Outline each blood parasite and name the species.
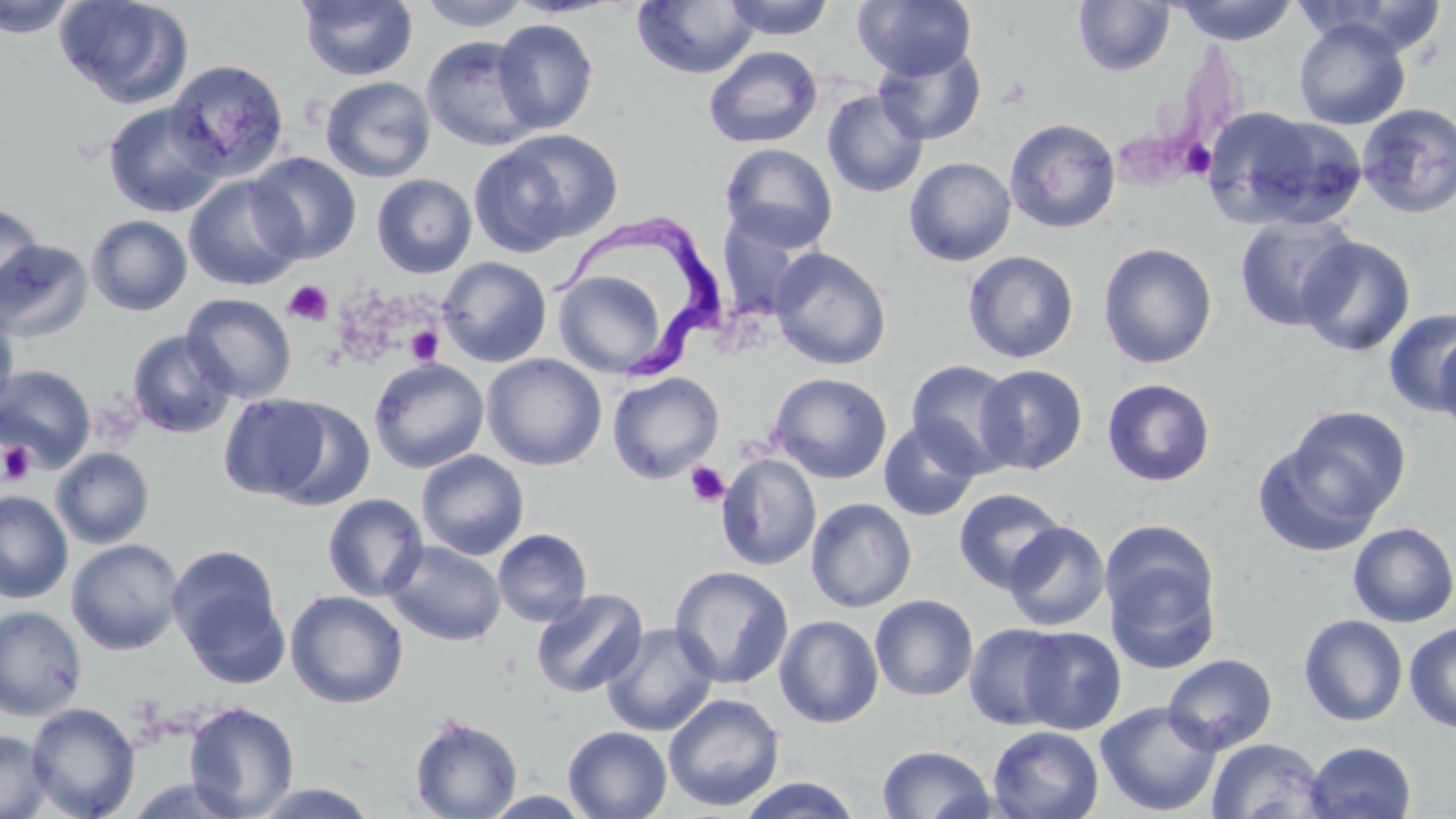
Approximate bounding boxes as [x1, y1, x2, y2] in pixels.
Trypanosoma brucei: [556, 214, 731, 383].
No Plasmodium falciparum, Plasmodium ovale, Plasmodium malariae, Plasmodium vivax, or Babesia divergens observed.

slide-level diagnosis = Trypanosoma brucei
field of view = single
magnification = 1000x
preparation = thin blood film
platelet locations = approximate bounding boxes as [x1, y1, x2, y2] in pixels: [1185, 132, 1219, 176], [283, 280, 333, 326], [405, 325, 443, 366], [2, 441, 36, 486], [685, 461, 730, 507]
modality = optical microscopy
image size = 1456×819 pixels
stain = May-Grünwald-Giemsa
uninfected red blood cell locations = approximate bounding boxes as [x1, y1, x2, y2] in pixels: [0, 0, 82, 38], [54, 0, 193, 108], [418, 0, 531, 31], [722, 0, 836, 40], [853, 0, 977, 81], [1170, 0, 1299, 45], [1294, 0, 1452, 57], [296, 1, 418, 81], [632, 1, 760, 79], [1073, 1, 1175, 76], [492, 18, 598, 134], [1294, 18, 1411, 131], [421, 35, 543, 151], [873, 43, 987, 145], [703, 45, 823, 148], [166, 59, 290, 180], [320, 76, 436, 183], [822, 89, 929, 198], [102, 102, 226, 217], [1357, 103, 1456, 218], [1214, 110, 1367, 231], [1003, 117, 1121, 233], [473, 129, 622, 252], [720, 143, 838, 253], [248, 152, 362, 264], [903, 157, 1017, 266], [183, 174, 306, 291], [371, 174, 477, 278], [0, 201, 47, 311], [716, 210, 818, 323], [1233, 213, 1359, 332], [85, 214, 193, 316], [1296, 235, 1416, 356], [0, 237, 97, 343], [1098, 242, 1217, 368], [769, 247, 892, 370], [963, 250, 1079, 363], [437, 257, 552, 367], [551, 260, 679, 380], [182, 293, 298, 403], [0, 307, 20, 418], [1383, 308, 1456, 415], [126, 330, 237, 439], [1433, 330, 1456, 435], [482, 353, 607, 470], [369, 358, 489, 473], [906, 359, 1023, 477], [975, 364, 1088, 475], [0, 365, 97, 472], [607, 371, 725, 483], [768, 372, 892, 484], [1102, 378, 1216, 487], [218, 393, 333, 501], [262, 398, 376, 511], [1285, 406, 1411, 519], [878, 418, 982, 522], [1251, 438, 1386, 556], [51, 447, 155, 548], [416, 450, 529, 560], [716, 453, 822, 571], [952, 487, 1067, 593], [0, 490, 73, 603], [322, 493, 429, 602], [805, 498, 917, 612], [1004, 521, 1110, 632], [1347, 521, 1456, 627], [492, 528, 592, 627], [66, 538, 185, 655], [384, 540, 506, 646], [167, 543, 288, 679], [1103, 543, 1222, 676], [669, 565, 794, 689], [531, 588, 648, 698], [285, 589, 409, 709], [870, 594, 978, 701], [0, 605, 87, 721], [1298, 614, 1408, 726], [774, 615, 884, 728], [601, 622, 719, 736], [1404, 622, 1456, 734], [964, 623, 1068, 730], [1019, 626, 1127, 734], [1163, 653, 1278, 755], [662, 693, 785, 812], [183, 700, 300, 818], [25, 701, 141, 819], [1095, 701, 1223, 816], [409, 714, 522, 819], [563, 726, 672, 818], [987, 726, 1104, 819], [0, 729, 53, 818], [1206, 738, 1327, 819], [1304, 741, 1417, 819], [877, 744, 995, 819], [735, 776, 864, 818], [248, 782, 383, 817]